Outline each uninfected red blood cell.
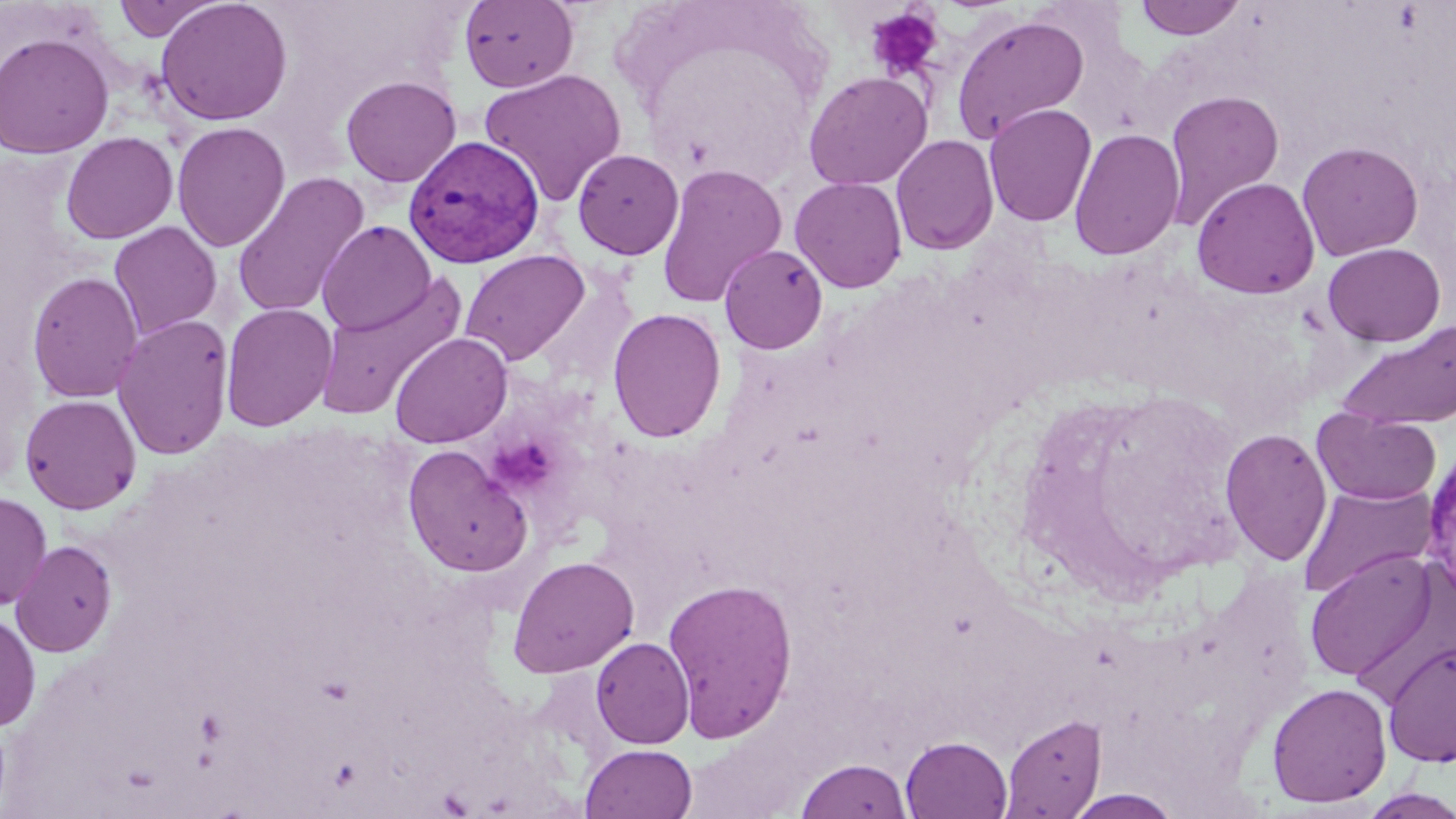

Approximate bounding boxes as [x1, y1, x2, y2] in pixels.
Uninfected red blood cells: [112, 0, 224, 41], [155, 0, 293, 126], [1133, 0, 1248, 40], [459, 1, 579, 92], [950, 13, 1089, 144], [0, 32, 115, 158], [479, 68, 627, 206], [803, 71, 933, 190], [340, 75, 462, 188], [1163, 89, 1285, 229], [984, 103, 1097, 227], [172, 121, 290, 252], [1068, 128, 1185, 260], [61, 132, 178, 244], [891, 134, 999, 255], [1297, 141, 1424, 261], [572, 149, 684, 260], [656, 162, 788, 308], [231, 172, 370, 318], [790, 176, 907, 293], [1191, 177, 1320, 299], [316, 220, 436, 336], [109, 221, 222, 339], [1322, 242, 1445, 346], [719, 244, 827, 354], [460, 249, 590, 365], [26, 270, 144, 403], [314, 271, 469, 422], [220, 303, 338, 432], [607, 308, 727, 443], [112, 314, 234, 460], [1336, 319, 1456, 431], [389, 332, 513, 448], [20, 394, 141, 514], [1312, 410, 1441, 505], [1220, 428, 1333, 566], [402, 444, 533, 578], [1297, 482, 1439, 599], [0, 492, 52, 610], [10, 539, 117, 657], [1304, 549, 1439, 683], [507, 555, 640, 678], [662, 577, 799, 742], [0, 613, 41, 731], [591, 636, 694, 748], [1382, 641, 1455, 768], [1267, 682, 1392, 807], [1001, 713, 1105, 818], [901, 736, 1013, 819], [580, 743, 698, 819], [795, 758, 913, 819], [1358, 788, 1456, 818], [1063, 789, 1184, 818].

Summary:
  - Plasmodium vivax-infected red blood cell locations: [404, 136, 545, 269], [1419, 443, 1456, 598]
  - Platelet locations: [864, 6, 943, 81], [488, 440, 555, 495]
  - Slide-level diagnosis: Plasmodium vivax
  - Modality: light microscopy
  - Magnification: 1000x
  - Field of view: single
  - Preparation: thin blood smear
  - Stain: May-Grünwald-Giemsa
  - Image size: 1456×819 pixels